Locate every Plasmodium parasite.
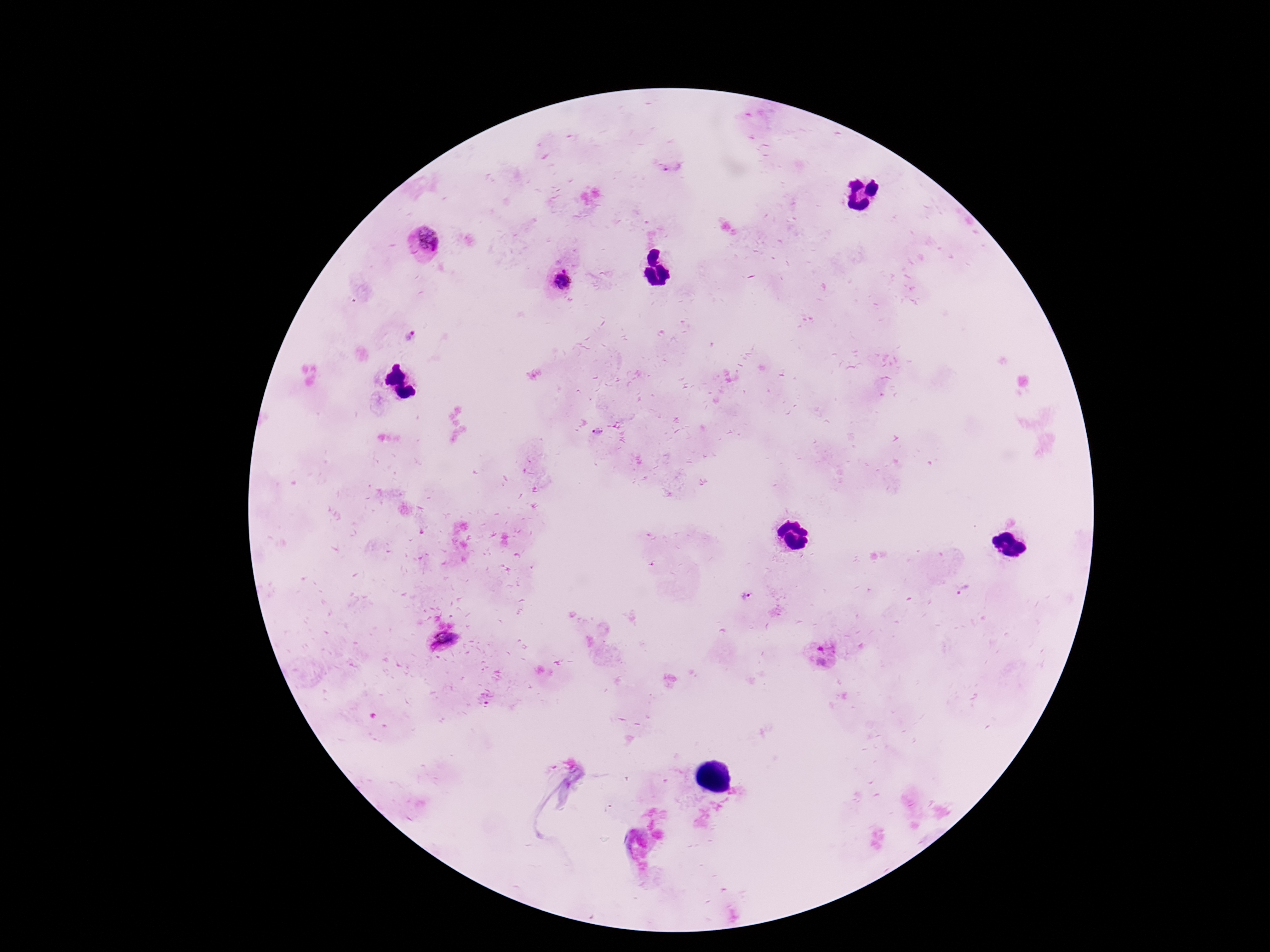
Approximate centers as [x, y] in pixels.
Plasmodium parasites: [673, 168], [425, 241], [563, 279], [410, 337], [598, 432], [963, 590], [746, 595], [442, 639], [822, 655].

patient malaria status = infected
capture = smartphone camera through the microscope eyepiece
image size = 1270×952 pixels
stain = Giemsa
field of view = one from this slide
magnification = 100x
preparation = thick blood smear